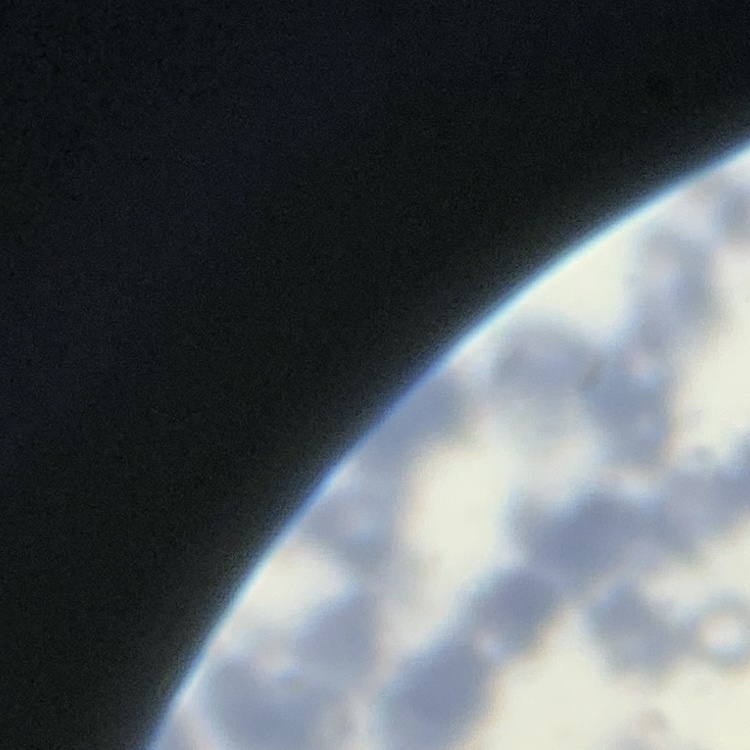
erythrocyte morphology = rouleaux formation
stain = Field's or Giemsa
image type = one tile cut from a larger photomicrograph
preparation = thin blood smear